Describe the morphology of the erythrocytes.
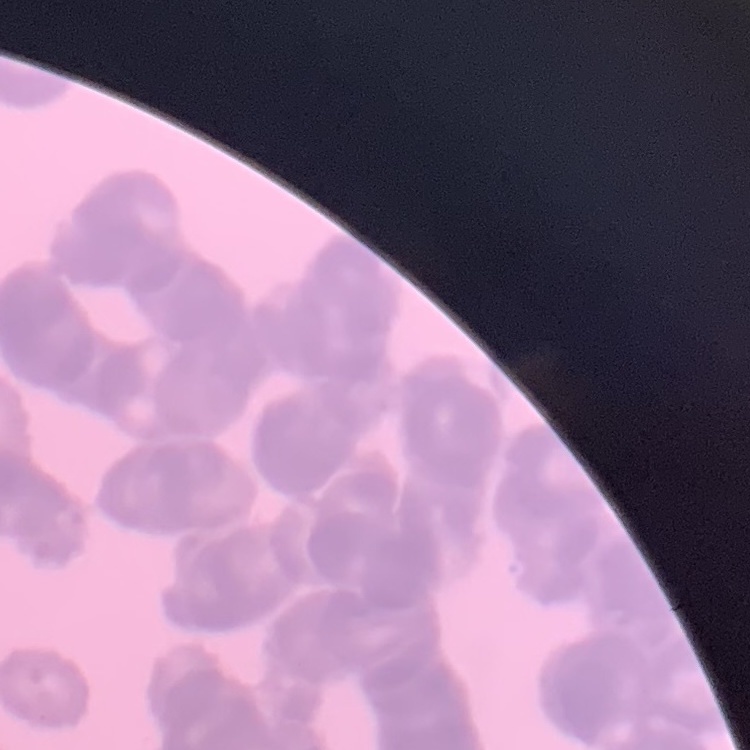

They show rouleaux formation.

Thin blood film. Square crop of a larger photomicrograph. Field's or Giemsa stain.